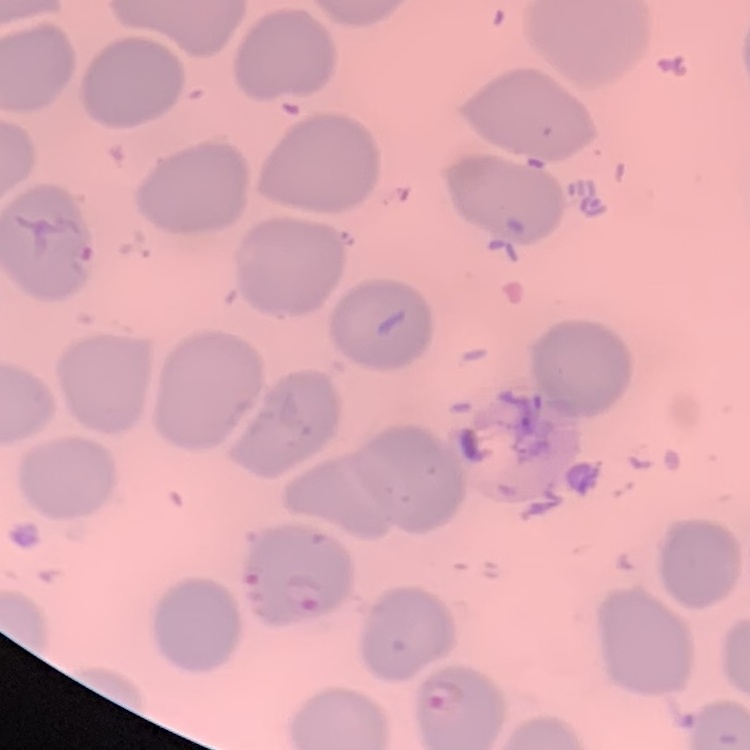 The erythrocytes show no rouleaux formation. Stained with either Field's or Giemsa. Thin blood film. Square crop of a larger photomicrograph.